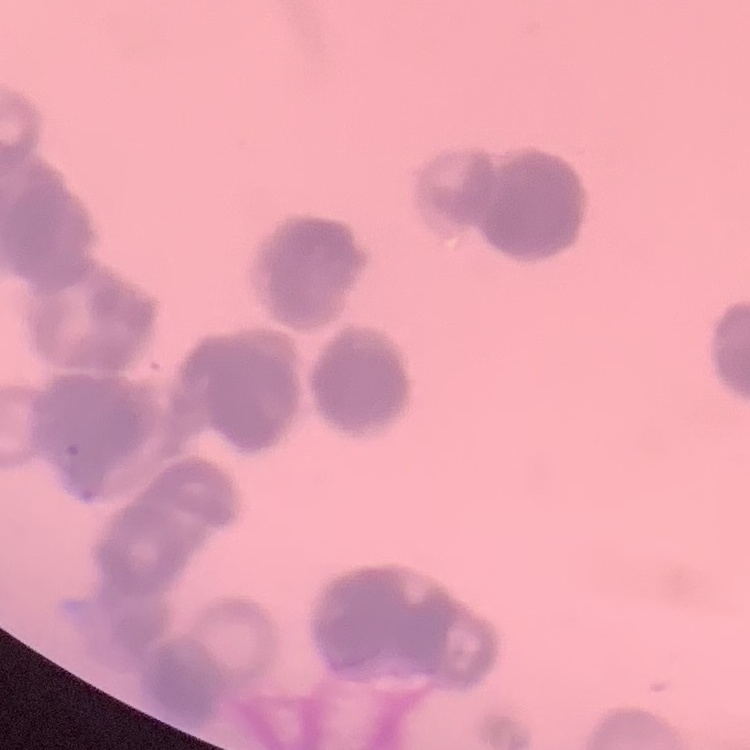
erythrocyte_morphology: rouleaux formation
stain: Field's or Giemsa
image_type: square crop of a larger photomicrograph
preparation: thin peripheral smear